Classify this cell by malaria status.
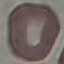
Uninfected.

stain = Giemsa
image type = automatically extracted cell patch, resized to 64 × 64 pixels
preparation = thin blood smear
capture = smartphone camera at the microscope eyepiece